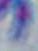

Toxoplasma gondii is shown. Micrograph. Captured at 1000x magnification.